Give the extent of all uninfected red blood cells.
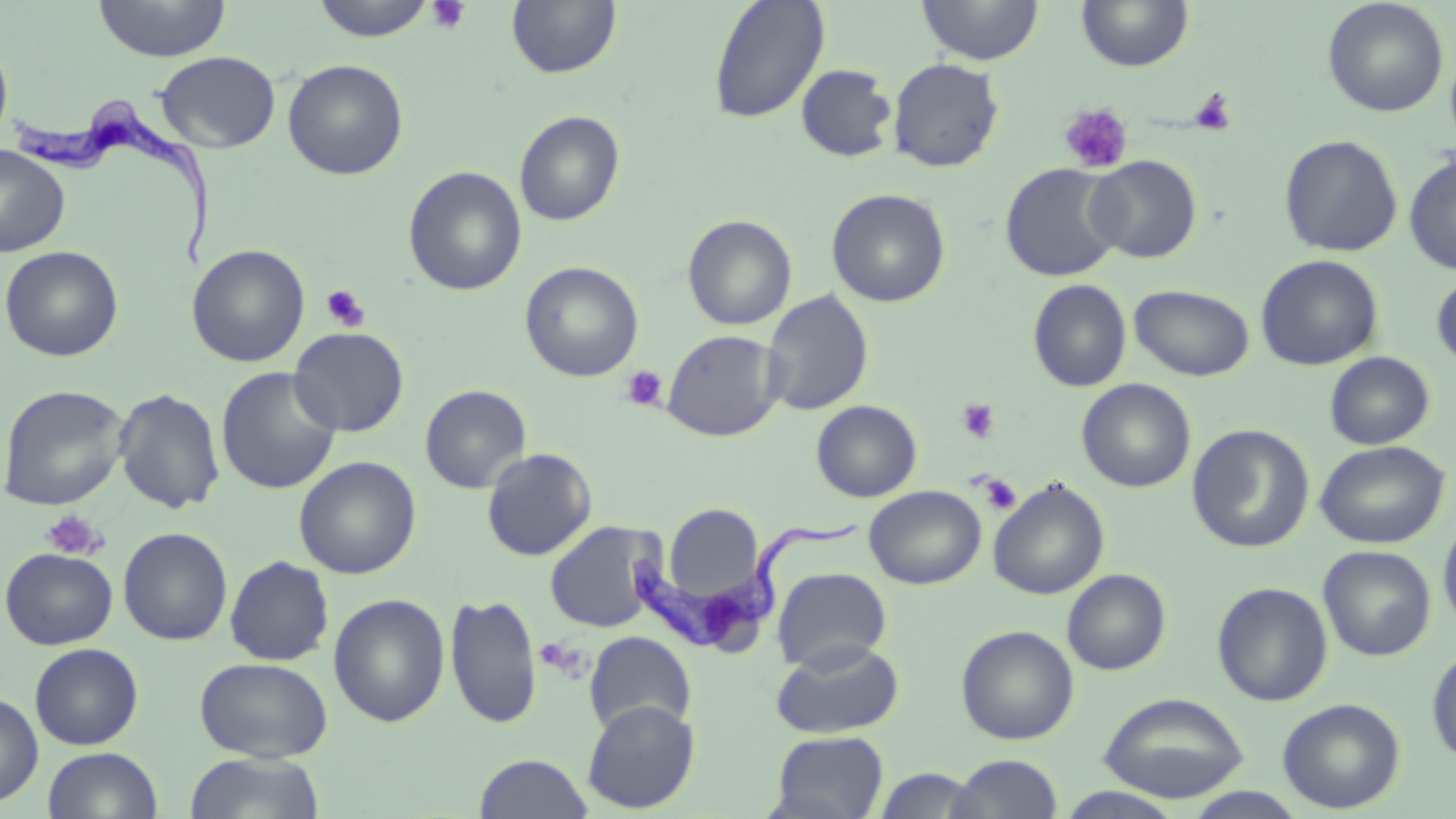
Approximate bounding boxes as named x1/y1/x2/y2 corners in pixels.
Uninfected red blood cells (subset): (x1=93, y1=0, x2=230, y2=62), (x1=310, y1=0, x2=438, y2=42), (x1=917, y1=0, x2=1043, y2=65), (x1=1323, y1=0, x2=1449, y2=118), (x1=506, y1=1, x2=622, y2=79), (x1=707, y1=1, x2=830, y2=124), (x1=0, y1=32, x2=13, y2=150), (x1=156, y1=51, x2=280, y2=153), (x1=888, y1=57, x2=1005, y2=172), (x1=282, y1=59, x2=409, y2=180), (x1=796, y1=63, x2=897, y2=162), (x1=514, y1=110, x2=625, y2=226), (x1=1279, y1=134, x2=1403, y2=257), (x1=0, y1=144, x2=70, y2=257), (x1=1404, y1=152, x2=1456, y2=275), (x1=1085, y1=155, x2=1202, y2=263), (x1=1000, y1=163, x2=1124, y2=282), (x1=403, y1=165, x2=527, y2=295), (x1=826, y1=188, x2=951, y2=308), (x1=682, y1=214, x2=797, y2=331), (x1=188, y1=244, x2=310, y2=367), (x1=0, y1=245, x2=123, y2=361), (x1=1256, y1=254, x2=1383, y2=371), (x1=520, y1=261, x2=643, y2=382), (x1=1431, y1=271, x2=1456, y2=370), (x1=1028, y1=279, x2=1131, y2=392), (x1=1129, y1=284, x2=1255, y2=381), (x1=761, y1=289, x2=874, y2=416), (x1=289, y1=326, x2=409, y2=437), (x1=662, y1=330, x2=785, y2=442), (x1=1324, y1=351, x2=1435, y2=450), (x1=215, y1=366, x2=342, y2=495), (x1=1076, y1=378, x2=1196, y2=493), (x1=0, y1=384, x2=129, y2=511), (x1=420, y1=384, x2=532, y2=493), (x1=113, y1=387, x2=226, y2=514), (x1=811, y1=400, x2=922, y2=502), (x1=1188, y1=424, x2=1315, y2=553), (x1=1315, y1=440, x2=1450, y2=549), (x1=482, y1=448, x2=597, y2=561), (x1=294, y1=456, x2=421, y2=579), (x1=988, y1=478, x2=1109, y2=600), (x1=865, y1=485, x2=986, y2=589), (x1=663, y1=504, x2=764, y2=604), (x1=1438, y1=515, x2=1456, y2=635), (x1=545, y1=520, x2=665, y2=633), (x1=118, y1=527, x2=233, y2=645), (x1=1318, y1=545, x2=1437, y2=661), (x1=1, y1=547, x2=118, y2=650), (x1=225, y1=555, x2=334, y2=666), (x1=772, y1=567, x2=891, y2=673), (x1=1062, y1=569, x2=1170, y2=675), (x1=1212, y1=581, x2=1333, y2=706), (x1=328, y1=593, x2=450, y2=727), (x1=444, y1=593, x2=543, y2=730), (x1=956, y1=624, x2=1079, y2=744), (x1=584, y1=631, x2=697, y2=736), (x1=770, y1=638, x2=904, y2=739), (x1=29, y1=642, x2=144, y2=749), (x1=1427, y1=644, x2=1456, y2=766), (x1=193, y1=657, x2=333, y2=761), (x1=0, y1=691, x2=43, y2=808), (x1=1098, y1=692, x2=1250, y2=803), (x1=1277, y1=698, x2=1406, y2=813), (x1=582, y1=699, x2=700, y2=814), (x1=769, y1=731, x2=890, y2=818), (x1=42, y1=746, x2=164, y2=819), (x1=182, y1=752, x2=325, y2=819), (x1=473, y1=753, x2=594, y2=819), (x1=948, y1=754, x2=1064, y2=818), (x1=873, y1=767, x2=983, y2=818), (x1=1053, y1=787, x2=1188, y2=818), (x1=1183, y1=788, x2=1312, y2=818).

Trypanosoma brucei locations: (x1=9, y1=92, x2=218, y2=269), (x1=619, y1=520, x2=858, y2=653). Platelet locations (subset): (x1=425, y1=0, x2=470, y2=34), (x1=1189, y1=88, x2=1237, y2=136), (x1=1059, y1=103, x2=1133, y2=174), (x1=321, y1=285, x2=371, y2=332), (x1=620, y1=365, x2=668, y2=411), (x1=957, y1=398, x2=1001, y2=444), (x1=978, y1=474, x2=1022, y2=515), (x1=41, y1=510, x2=106, y2=560), (x1=534, y1=638, x2=585, y2=678). Slide-level diagnosis: Trypanosoma brucei. May-Grünwald-Giemsa stain. Image is 1456×819 pixels. Light microscopy. Single field of view. Captured at 1000x magnification. Thin blood film.